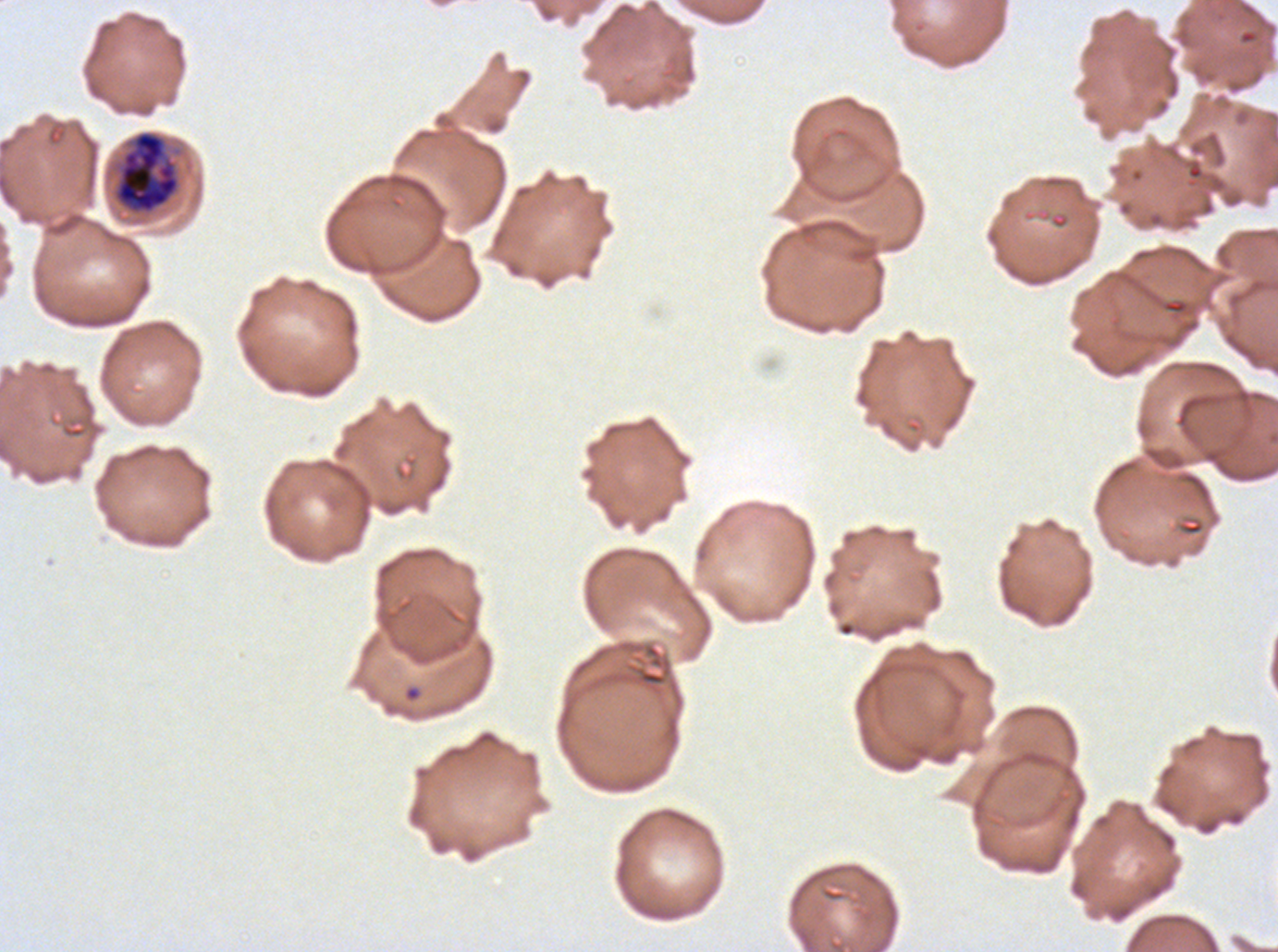

early_schizont_locations: 'approximate bounding rectangles given as corner coordinates in pixels from the top-left: (x1=114, y1=130, x2=180, y2=214)'
specimen: P. falciparum cultured ex vivo for 24 to 48 hours, from a patient in The Gambia
stain: Giemsa
field_of_view: one sub-image of a larger composite
preparation: thin blood film
image_size: 1278×952 pixels